Locate and identify every blood parasite.
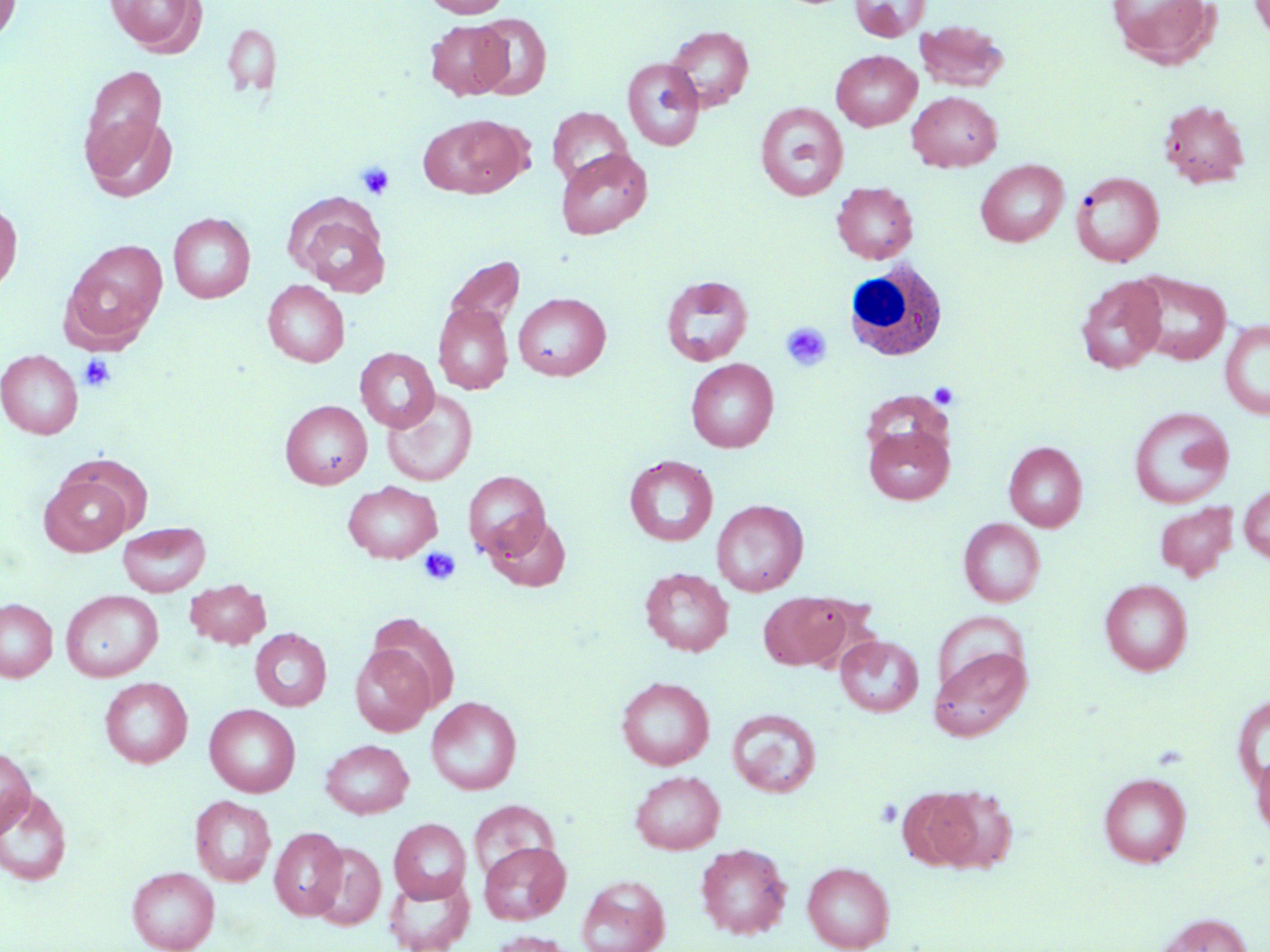
No blood parasites observed.

Summary:
  - Coordinate format: approximate bounding boxes as (x1, y1, x2, y2) in pixels
  - White blood cell locations: (843, 260, 949, 361)
  - Uninfected red blood cell locations: (0, 0, 21, 44), (106, 0, 206, 56), (423, 0, 511, 17), (850, 0, 929, 42), (1107, 0, 1218, 67), (1249, 0, 1270, 42), (471, 13, 552, 99), (426, 20, 512, 99), (914, 20, 1010, 92), (222, 23, 282, 97), (664, 26, 754, 111), (831, 50, 922, 131), (622, 58, 705, 151), (80, 65, 167, 166), (906, 91, 1002, 171), (1159, 99, 1250, 188), (755, 102, 849, 201), (547, 107, 633, 186), (83, 112, 178, 201), (419, 115, 530, 198), (555, 148, 652, 239), (975, 160, 1068, 247), (1071, 171, 1164, 267), (832, 183, 918, 263), (0, 199, 22, 295), (290, 201, 391, 296), (168, 213, 255, 303), (61, 240, 168, 352), (443, 255, 526, 336), (1130, 271, 1231, 365), (1076, 274, 1166, 373), (660, 275, 754, 366), (262, 280, 350, 367), (514, 293, 611, 380), (433, 303, 513, 395), (1219, 320, 1270, 419), (355, 347, 439, 432), (1, 349, 83, 439), (686, 358, 779, 452), (382, 389, 478, 486), (860, 391, 953, 464), (280, 400, 372, 489), (1129, 406, 1234, 508), (863, 423, 955, 505), (1004, 441, 1087, 531), (624, 455, 718, 546), (463, 470, 550, 560), (39, 473, 134, 556), (343, 481, 442, 563), (1239, 484, 1270, 565), (711, 500, 808, 596), (1154, 501, 1238, 580), (486, 513, 571, 592), (958, 518, 1045, 606), (117, 521, 211, 596), (640, 568, 733, 656), (184, 579, 271, 649), (1100, 579, 1193, 675), (61, 590, 163, 681), (758, 592, 855, 671), (0, 598, 58, 682), (250, 628, 332, 712), (835, 635, 923, 716), (350, 644, 435, 736), (929, 646, 1032, 741), (616, 676, 714, 770), (100, 677, 192, 768), (1233, 692, 1270, 792), (426, 696, 522, 795), (204, 704, 300, 797), (727, 708, 822, 798), (320, 739, 414, 818), (0, 745, 36, 838), (1251, 751, 1270, 840), (630, 770, 725, 854), (1099, 772, 1192, 867), (917, 785, 1019, 873), (0, 788, 72, 886), (189, 795, 276, 887), (469, 801, 559, 882), (389, 819, 472, 903), (270, 827, 347, 920), (479, 841, 570, 924), (308, 842, 386, 930), (695, 843, 792, 940), (802, 861, 895, 951), (127, 866, 220, 952), (383, 873, 474, 952), (576, 874, 670, 952), (1154, 913, 1254, 952), (488, 930, 574, 952)
  - Platelet locations: (356, 161, 395, 201), (781, 322, 832, 371), (78, 354, 116, 392), (929, 382, 959, 409), (419, 547, 461, 586), (875, 798, 903, 828)
  - Slide-level diagnosis: no evidence of blood parasites
  - Field of view: one of a larger specimen
  - Preparation: thin blood smear
  - Image size: 1270×952 pixels
  - Modality: light microscopy
  - Stain: May-Grünwald-Giemsa
  - Magnification: 1000x